Mark where leukocytes are.
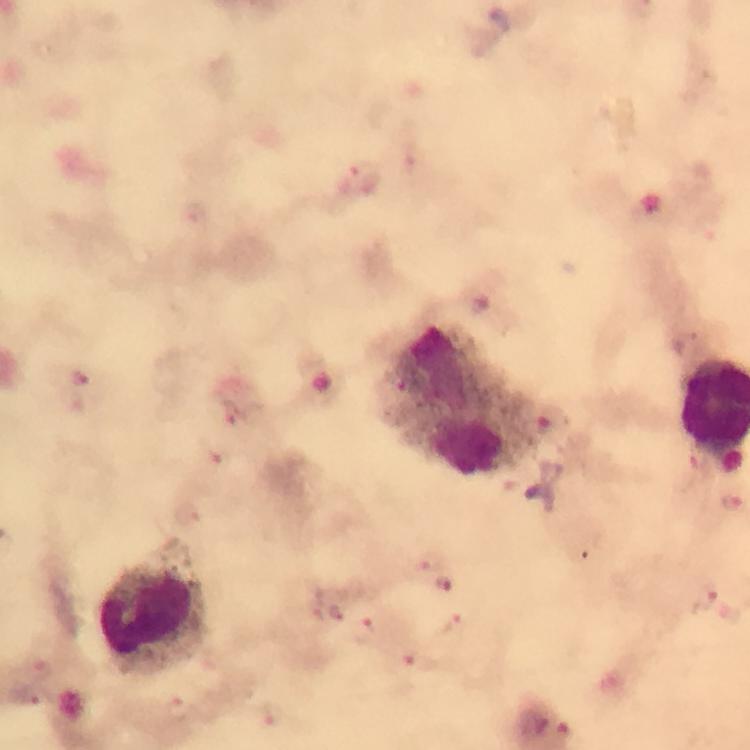
Approximate object centers, in pixels from the top-left corner.
Leukocytes: (x=461, y=400), (x=154, y=608).

image_size: 750×750 pixels
malaria_parasite_locations: 'approximate object centers, in pixels from the top-left corner: (x=363, y=175), (x=78, y=379), (x=218, y=454), (x=186, y=512), (x=431, y=560), (x=447, y=583), (x=705, y=596), (x=452, y=627), (x=363, y=631), (x=423, y=663), (x=38, y=668), (x=176, y=709), (x=273, y=715)'
magnification: 100x
capture: smartphone camera through the microscope
preparation: thick smear
context: from a diagnostic examination for malaria
stain: Giemsa
immersion_oil: applied
cropped_from: a single field of view